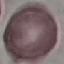
Summary:
  - Malaria status: uninfected
  - Image type: cell patch, automatically extracted from a larger field of view and resized to 64 × 64 pixels
  - Capture: smartphone through the microscope eyepiece
  - Stain: Giemsa
  - Preparation: thin smear